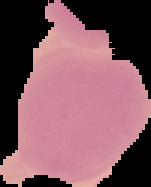
image type = cell region segmented out of the field of view; surrounding area masked to black
preparation = thin blood film
image size = 151×187 pixels
malaria status = uninfected